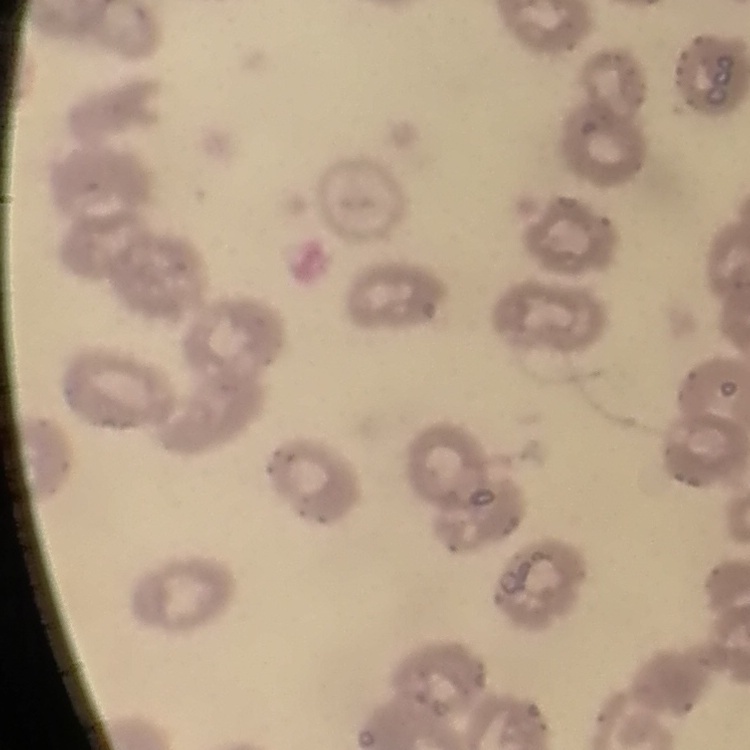

The erythrocytes show no rouleaux formation. Thin peripheral smear. One tile cut from a larger photomicrograph. Stained with either Field's or Giemsa.